Give the extent of all Plasmodium vivax-infected red blood cells.
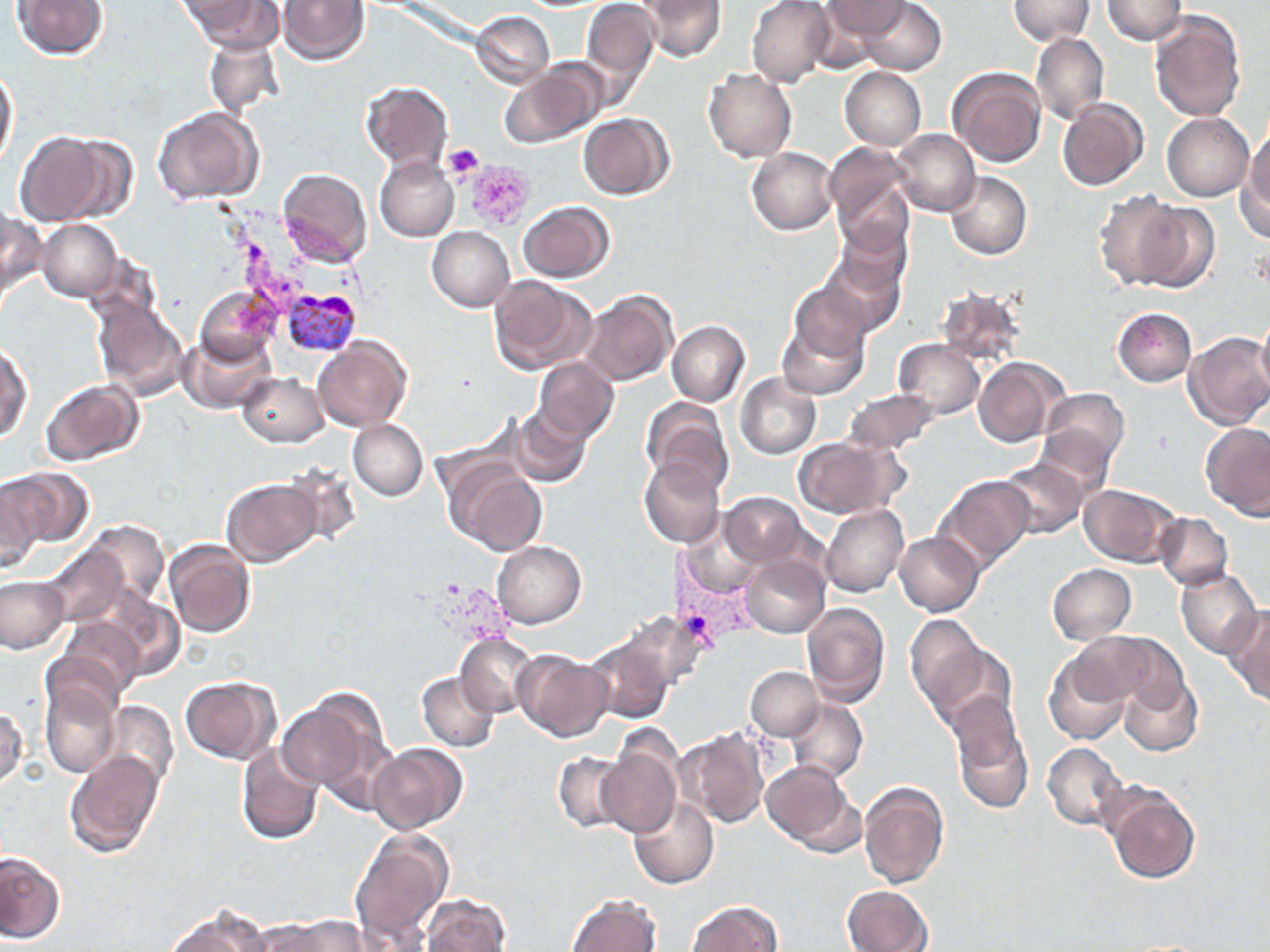

Approximate bounding boxes as [x1, y1, x2, y2] in pixels.
Plasmodium vivax-infected red blood cells: [280, 288, 362, 358], [658, 542, 757, 658].

Summary:
  - Uninfected red blood cell locations: [13, 0, 106, 58], [180, 0, 279, 51], [581, 0, 659, 96], [639, 0, 726, 62], [747, 0, 832, 86], [856, 0, 946, 75], [1007, 0, 1095, 43], [1103, 0, 1186, 44], [279, 1, 369, 65], [821, 1, 911, 38], [1150, 10, 1245, 124], [471, 11, 554, 88], [1031, 31, 1108, 124], [203, 33, 284, 117], [497, 61, 603, 150], [1, 64, 18, 166], [840, 67, 926, 151], [948, 67, 1045, 168], [704, 69, 797, 163], [360, 82, 453, 169], [1058, 99, 1148, 192], [152, 108, 263, 205], [1163, 112, 1254, 201], [578, 113, 673, 199], [1240, 127, 1270, 239], [892, 129, 980, 216], [15, 131, 104, 226], [55, 135, 139, 223], [826, 145, 916, 250], [747, 147, 837, 234], [375, 155, 459, 240], [277, 168, 372, 267], [945, 171, 1032, 260], [1094, 189, 1186, 290], [519, 202, 614, 282], [1132, 202, 1220, 293], [1, 210, 44, 303], [38, 219, 121, 301], [427, 226, 515, 312], [817, 242, 907, 337], [488, 275, 595, 374], [790, 279, 875, 360], [197, 285, 282, 369], [934, 285, 1026, 369], [582, 290, 678, 387], [92, 297, 190, 400], [1113, 307, 1196, 386], [1255, 312, 1270, 400], [777, 314, 868, 400], [667, 321, 749, 406], [182, 331, 278, 413], [1182, 332, 1270, 430], [312, 337, 411, 432], [895, 339, 985, 417], [1, 343, 32, 440], [534, 357, 618, 441], [975, 357, 1066, 446], [237, 373, 328, 447], [736, 373, 821, 459], [41, 379, 144, 465], [845, 388, 939, 453], [1040, 388, 1129, 468], [641, 397, 733, 493], [509, 405, 592, 488], [348, 420, 428, 501], [1201, 423, 1270, 519], [1030, 426, 1116, 502], [791, 436, 906, 517], [640, 458, 726, 549], [995, 458, 1088, 538], [447, 461, 548, 556], [7, 468, 94, 546], [935, 475, 1034, 572], [0, 477, 43, 574], [221, 477, 321, 566], [1079, 483, 1180, 566], [721, 492, 806, 566], [822, 504, 908, 597], [1155, 513, 1233, 590], [681, 516, 763, 596], [82, 519, 169, 610], [894, 532, 985, 617], [164, 540, 256, 640], [491, 541, 586, 627], [41, 545, 129, 627], [741, 555, 830, 638], [1046, 564, 1135, 644], [1176, 568, 1261, 658], [0, 576, 67, 653], [99, 589, 185, 680], [800, 601, 889, 706], [1226, 607, 1270, 704], [617, 610, 711, 692], [903, 613, 989, 715], [54, 617, 144, 704], [1074, 630, 1184, 713], [456, 632, 539, 717], [586, 636, 673, 723], [927, 640, 1017, 735], [515, 650, 612, 741], [1044, 653, 1132, 745], [745, 666, 821, 740], [417, 671, 499, 752], [1117, 671, 1201, 756], [180, 676, 280, 763], [41, 679, 120, 779], [279, 691, 384, 798], [786, 698, 867, 783], [101, 701, 178, 791], [0, 704, 27, 791], [950, 706, 1034, 814], [676, 727, 769, 827], [596, 737, 681, 837], [1042, 742, 1126, 830], [236, 743, 323, 844], [369, 743, 468, 835], [64, 750, 166, 858], [552, 752, 632, 833], [761, 760, 856, 852], [858, 780, 949, 888], [1104, 782, 1200, 884], [628, 794, 719, 889], [351, 826, 453, 948], [0, 850, 65, 943], [843, 885, 933, 952], [566, 893, 661, 952], [422, 894, 511, 952], [687, 901, 781, 951], [163, 907, 271, 952], [269, 916, 373, 952]
  - Platelet locations: [443, 143, 485, 182], [462, 159, 535, 229]
  - Slide-level diagnosis: Plasmodium vivax
  - Preparation: thin blood film
  - Modality: optical microscopy
  - Field of view: single
  - Stain: May-Grünwald-Giemsa
  - Magnification: 1000x
  - Image size: 1270×952 pixels